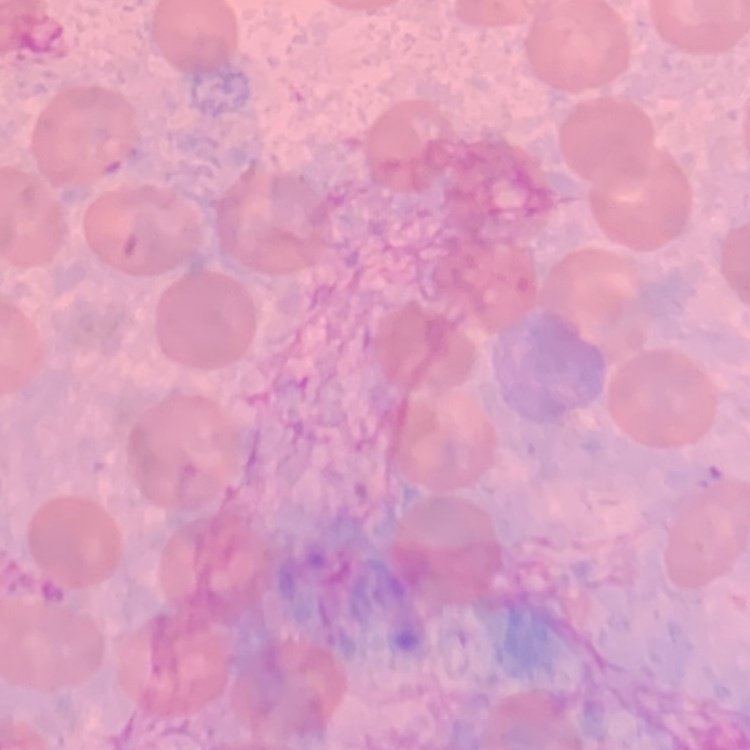

The erythrocytes exhibit no rouleaux formation. Square crop of a larger photomicrograph. Field's or Giemsa stain. Thin blood film.